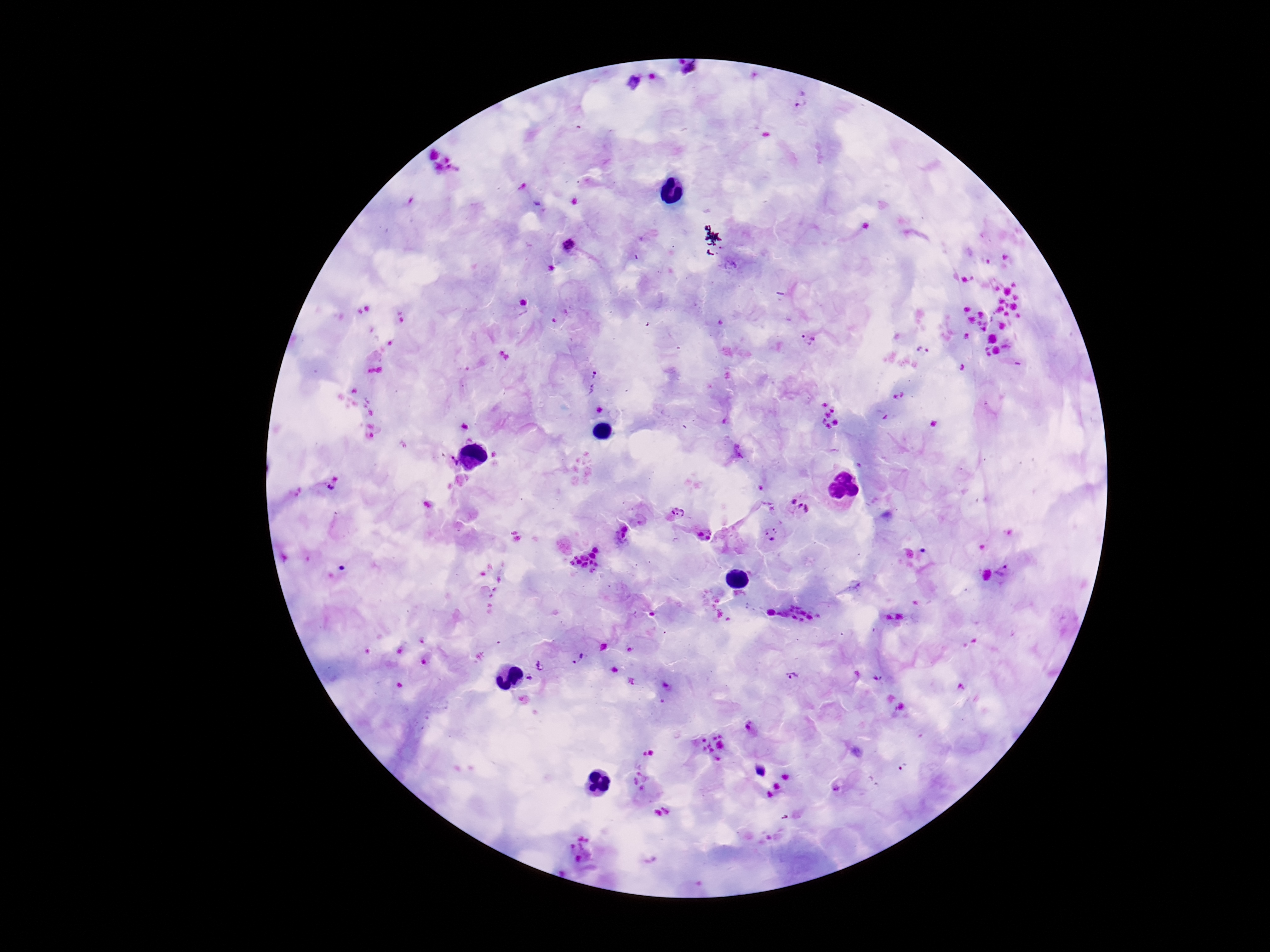

{
  "preparation": "thick peripheral-blood smear",
  "image_size": "1270×952 pixels",
  "stain": "Giemsa",
  "capture": "smartphone camera through the microscope eyepiece",
  "field_of_view": "single",
  "patient_malaria_status": "infected",
  "magnification": "100x",
  "plasmodium_parasite_locations": "approximate centers as [x, y] in pixels: [800, 99], [569, 246], [522, 303], [808, 339], [922, 351], [593, 381], [453, 464], [329, 489], [790, 499], [803, 511], [676, 513], [777, 528], [706, 535], [768, 540], [1005, 575], [578, 658], [541, 666], [792, 675], [530, 682], [751, 729], [838, 787]"
}